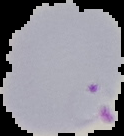 Cell region segmented out of the field of view; the surrounding area is masked to black. From a thin blood film. Image is 124×136 pixels. Result: malaria parasites identified.